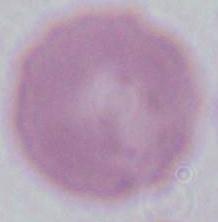
Captured at 1000x magnification. An erythrocyte is shown. Micrograph.